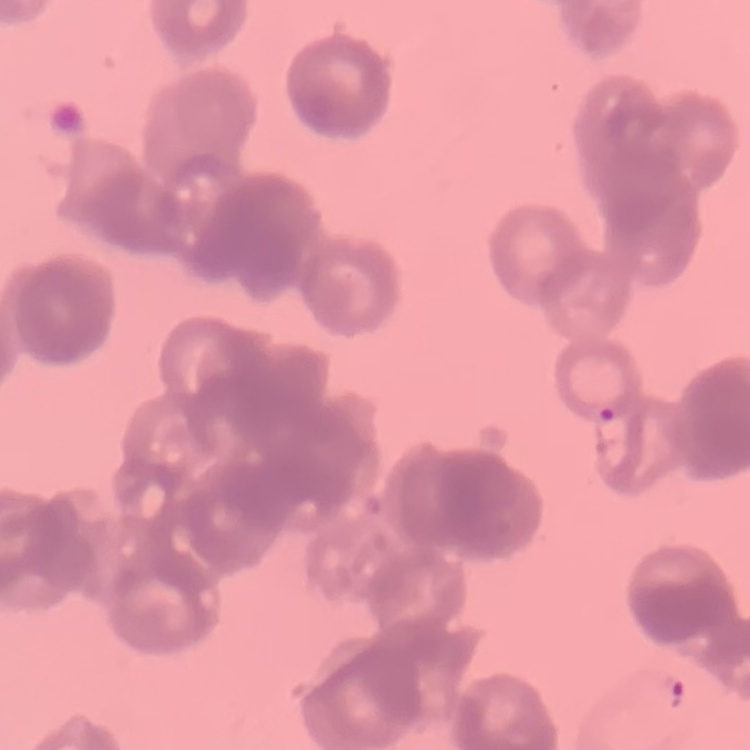 The red blood cells exhibit rouleaux formation. Thin blood smear. Square crop of a larger photomicrograph. Field's or Giemsa stain.